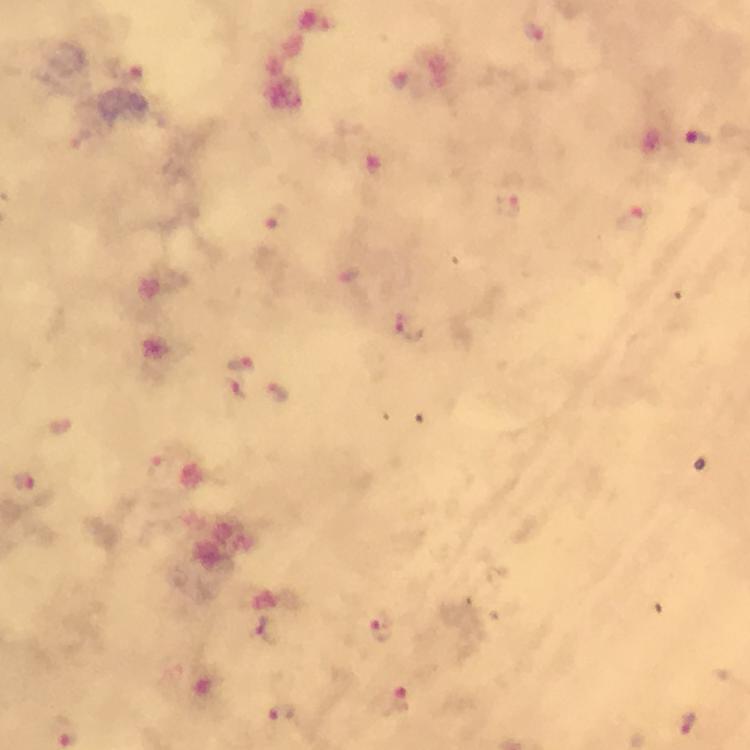
Approximate centers as [x, y] in pixels. Plasmodium parasite locations: [699, 138], [276, 217], [634, 219], [409, 329], [240, 364], [239, 390], [279, 393], [25, 482], [381, 627], [269, 630], [396, 702], [284, 715], [687, 724]. Immersion oil applied. Photographed with a smartphone mounted on the microscope. Giemsa stain. Thick blood smear. From a diagnostic examination for malaria. Cropped region of a single field of view. Image is 750×750 pixels. 100x magnification.